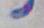

{
  "magnification": "1000x",
  "modality": "photomicrograph",
  "identification": "Toxoplasma gondii"
}